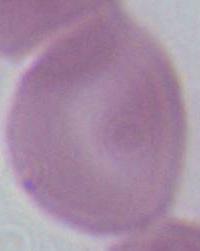
Summary:
  - Modality: photomicrograph
  - Magnification: 1000x
  - Identification: erythrocyte